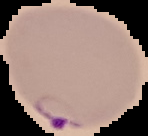 The area outside the segmented cell region is set to black. From a thin blood smear. Image is 148×136 pixels. Malaria status: parasitized.